State which parasite is depicted.
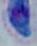
This is Toxoplasma gondii.

Summary:
  - Modality: photomicrograph
  - Magnification: 1000x